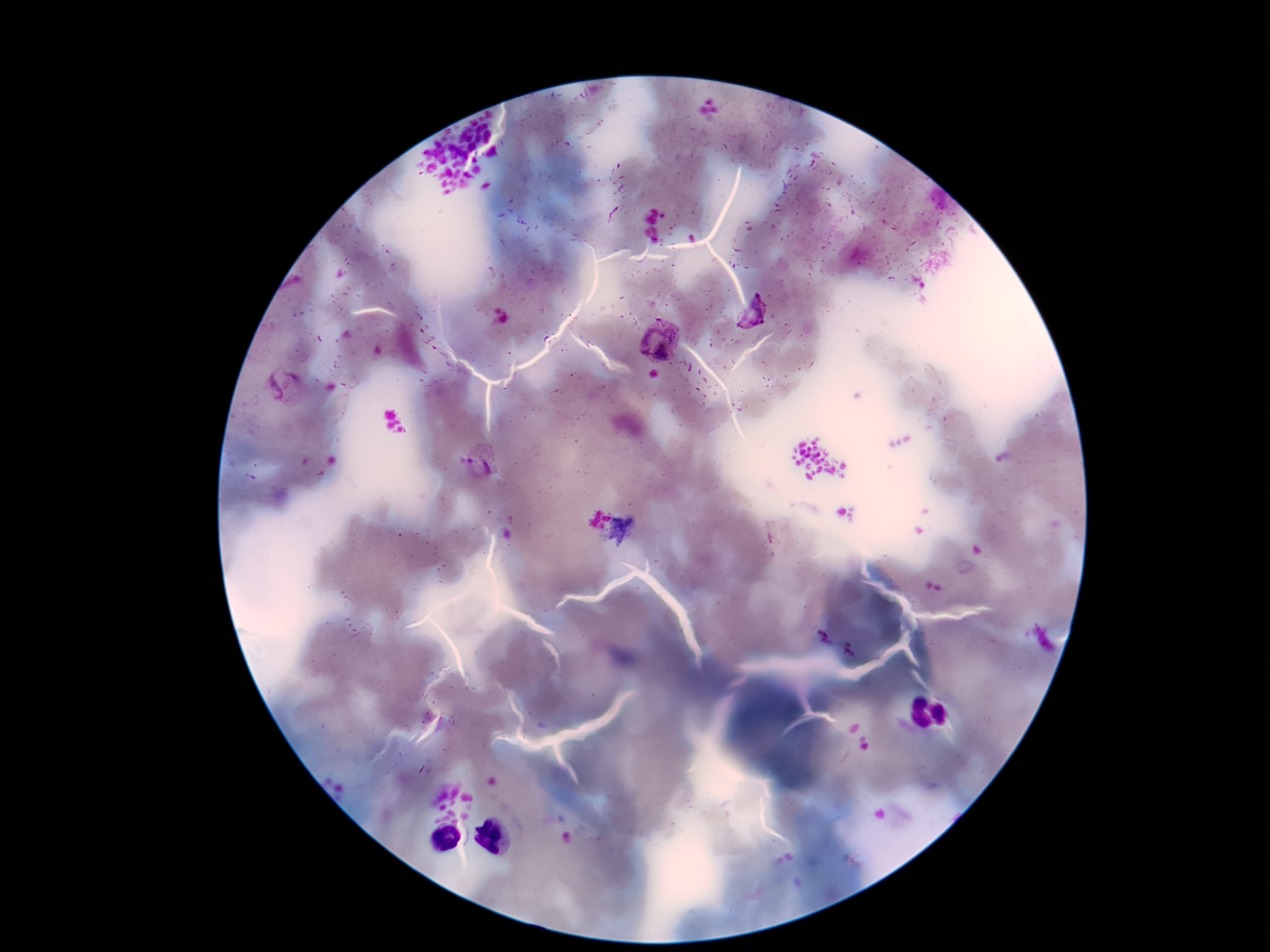
Approximate centers as {x, y} in pixels.
Summary:
  - Plasmodium parasite locations: {754, 316}, {660, 340}, {284, 386}, {485, 461}
  - Preparation: thick blood smear
  - Capture: smartphone camera through the microscope eyepiece
  - Field of view: one from this slide
  - Patient malaria status: infected
  - Stain: Giemsa
  - Magnification: 100x
  - Image size: 1270×952 pixels